Give the extent of all uninfected red blood cells.
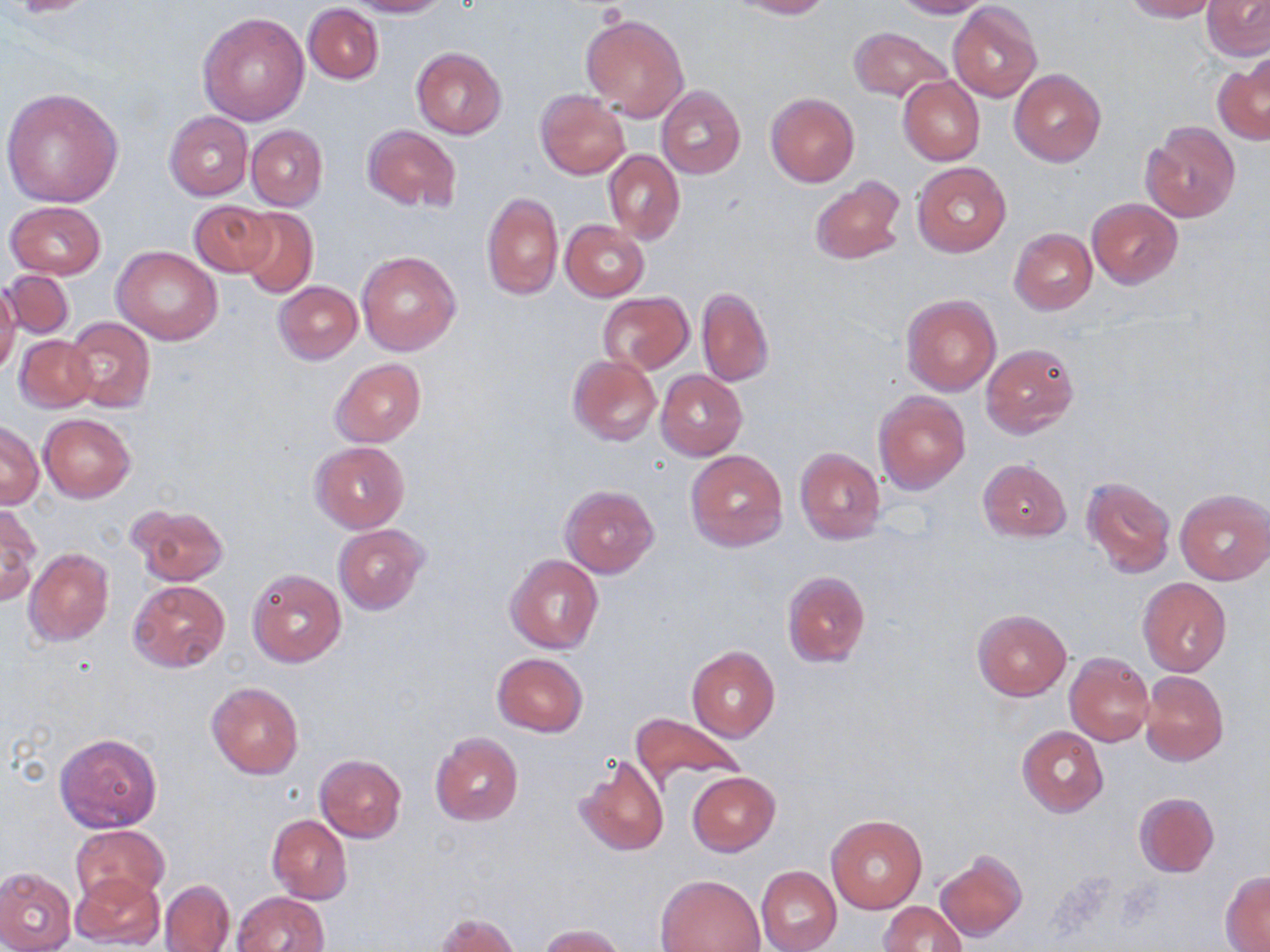

Approximate bounding boxes as named x1/y1/x2/y2 corners in pixels.
Uninfected red blood cells: (x1=4, y1=0, x2=107, y2=17), (x1=349, y1=0, x2=451, y2=17), (x1=731, y1=0, x2=832, y2=19), (x1=891, y1=0, x2=993, y2=19), (x1=1121, y1=0, x2=1219, y2=22), (x1=1203, y1=0, x2=1270, y2=62), (x1=947, y1=3, x2=1043, y2=101), (x1=303, y1=4, x2=384, y2=84), (x1=197, y1=12, x2=309, y2=126), (x1=580, y1=14, x2=688, y2=123), (x1=847, y1=26, x2=953, y2=102), (x1=411, y1=48, x2=506, y2=138), (x1=1213, y1=57, x2=1270, y2=146), (x1=1007, y1=68, x2=1106, y2=166), (x1=898, y1=76, x2=985, y2=165), (x1=657, y1=85, x2=745, y2=179), (x1=2, y1=87, x2=124, y2=209), (x1=536, y1=90, x2=630, y2=179), (x1=766, y1=92, x2=859, y2=187), (x1=165, y1=111, x2=253, y2=200), (x1=1142, y1=121, x2=1240, y2=221), (x1=246, y1=124, x2=328, y2=212), (x1=361, y1=124, x2=463, y2=213), (x1=603, y1=150, x2=684, y2=244), (x1=912, y1=162, x2=1011, y2=257), (x1=810, y1=175, x2=907, y2=266), (x1=481, y1=191, x2=562, y2=301), (x1=1087, y1=198, x2=1183, y2=288), (x1=4, y1=200, x2=107, y2=279), (x1=189, y1=200, x2=276, y2=277), (x1=237, y1=207, x2=318, y2=297), (x1=561, y1=220, x2=650, y2=301), (x1=1009, y1=228, x2=1096, y2=315), (x1=111, y1=246, x2=222, y2=346), (x1=356, y1=251, x2=461, y2=357), (x1=2, y1=270, x2=73, y2=340), (x1=273, y1=281, x2=362, y2=364), (x1=0, y1=282, x2=21, y2=377), (x1=697, y1=288, x2=773, y2=386), (x1=597, y1=293, x2=693, y2=374), (x1=900, y1=295, x2=1001, y2=397), (x1=66, y1=316, x2=155, y2=413), (x1=13, y1=335, x2=98, y2=413), (x1=981, y1=342, x2=1080, y2=440), (x1=567, y1=354, x2=662, y2=446), (x1=330, y1=358, x2=426, y2=447), (x1=656, y1=370, x2=746, y2=460), (x1=873, y1=391, x2=971, y2=493), (x1=39, y1=413, x2=136, y2=502), (x1=1, y1=421, x2=43, y2=510), (x1=310, y1=440, x2=410, y2=533), (x1=796, y1=447, x2=885, y2=544), (x1=684, y1=450, x2=789, y2=552), (x1=978, y1=458, x2=1071, y2=541), (x1=1082, y1=476, x2=1175, y2=578), (x1=560, y1=485, x2=659, y2=578), (x1=1175, y1=490, x2=1270, y2=585), (x1=1, y1=501, x2=41, y2=605), (x1=128, y1=504, x2=228, y2=585), (x1=333, y1=524, x2=428, y2=614), (x1=23, y1=548, x2=114, y2=647), (x1=505, y1=554, x2=603, y2=653), (x1=247, y1=569, x2=346, y2=667), (x1=782, y1=570, x2=870, y2=668), (x1=1137, y1=578, x2=1232, y2=675), (x1=128, y1=579, x2=230, y2=673), (x1=972, y1=609, x2=1071, y2=700), (x1=686, y1=646, x2=780, y2=741), (x1=492, y1=652, x2=588, y2=737), (x1=1065, y1=653, x2=1154, y2=746), (x1=1141, y1=670, x2=1229, y2=767), (x1=206, y1=681, x2=304, y2=778), (x1=633, y1=713, x2=743, y2=791), (x1=1016, y1=726, x2=1109, y2=817), (x1=54, y1=732, x2=162, y2=833), (x1=430, y1=733, x2=523, y2=826), (x1=576, y1=751, x2=669, y2=857), (x1=315, y1=754, x2=406, y2=842), (x1=687, y1=772, x2=780, y2=855), (x1=1134, y1=792, x2=1220, y2=878), (x1=826, y1=814, x2=927, y2=914), (x1=267, y1=815, x2=352, y2=905), (x1=71, y1=824, x2=169, y2=905), (x1=934, y1=849, x2=1027, y2=943), (x1=756, y1=866, x2=840, y2=951), (x1=0, y1=867, x2=76, y2=952), (x1=1221, y1=871, x2=1270, y2=951), (x1=71, y1=872, x2=165, y2=950), (x1=655, y1=874, x2=764, y2=952), (x1=161, y1=879, x2=234, y2=951), (x1=233, y1=891, x2=329, y2=952), (x1=880, y1=901, x2=967, y2=952), (x1=436, y1=913, x2=518, y2=951), (x1=538, y1=923, x2=627, y2=951).

{
  "slide_level_diagnosis": "negative for blood parasites",
  "image_size": "1270×952 pixels",
  "preparation": "thin blood smear",
  "stain": "May-Grünwald-Giemsa",
  "magnification": "1000x",
  "field_of_view": "one of a larger specimen",
  "modality": "light microscopy"
}